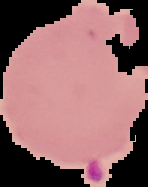
Summary:
  - Preparation: thin blood smear
  - Result: Plasmodium parasites detected
  - Image type: segmented cell region with the area outside set to black
  - Image size: 148×187 pixels